Identify the parasite.
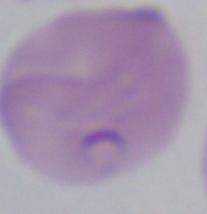

This is Babesia.

Summary:
  - Modality: micrograph
  - Magnification: 1000x